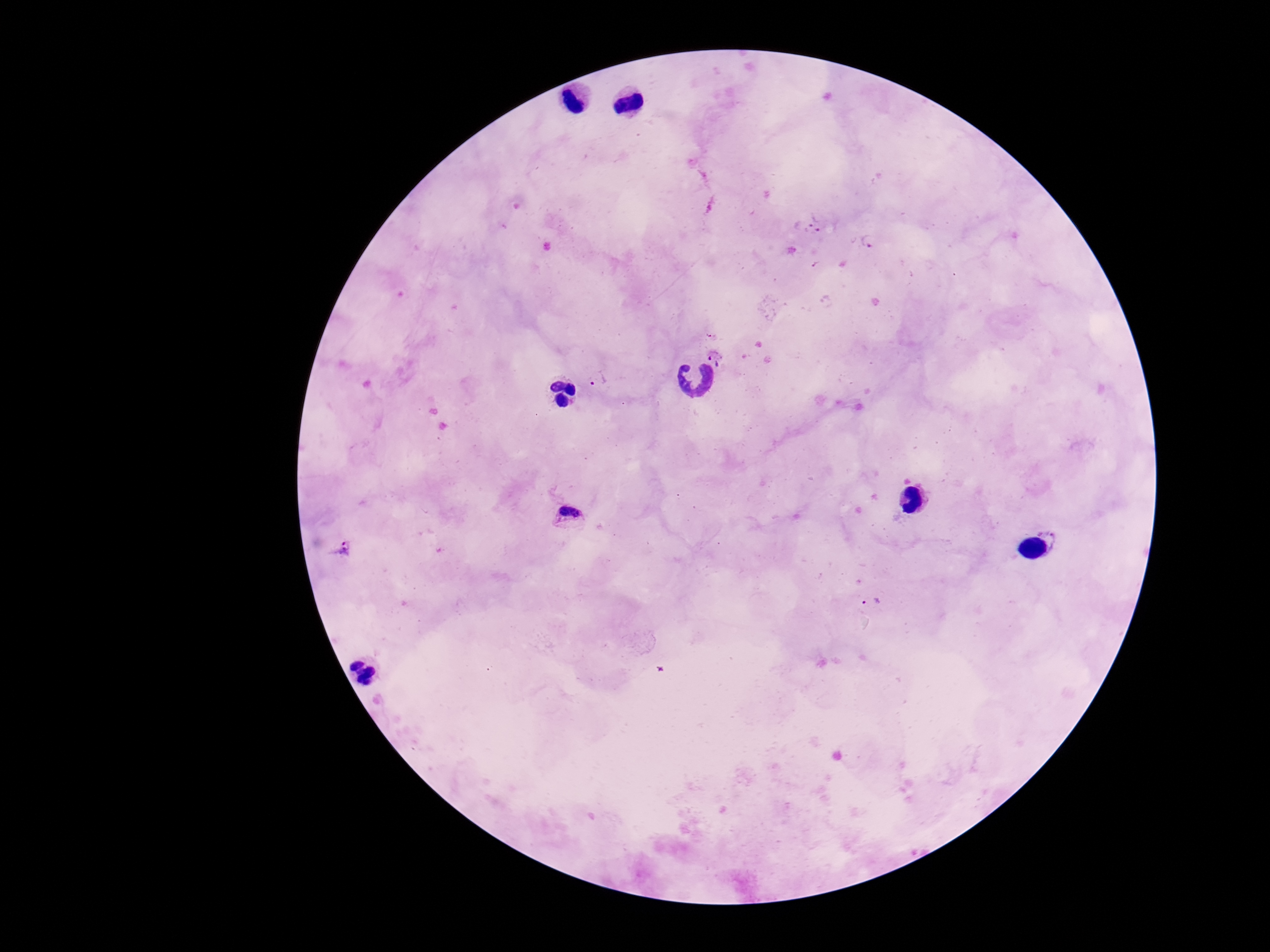
Approximate object centers, in pixels from the top-left corner. Plasmodium parasite locations: (x=822, y=220), (x=804, y=226), (x=869, y=241), (x=711, y=332), (x=716, y=357), (x=598, y=378), (x=570, y=513), (x=345, y=547), (x=872, y=602). 100x magnification. Image is 1270×952 pixels. Patient malaria status: positive. Photographed through the microscope eyepiece with a smartphone camera. One field from this slide. Thick blood smear. Giemsa-stained preparation.